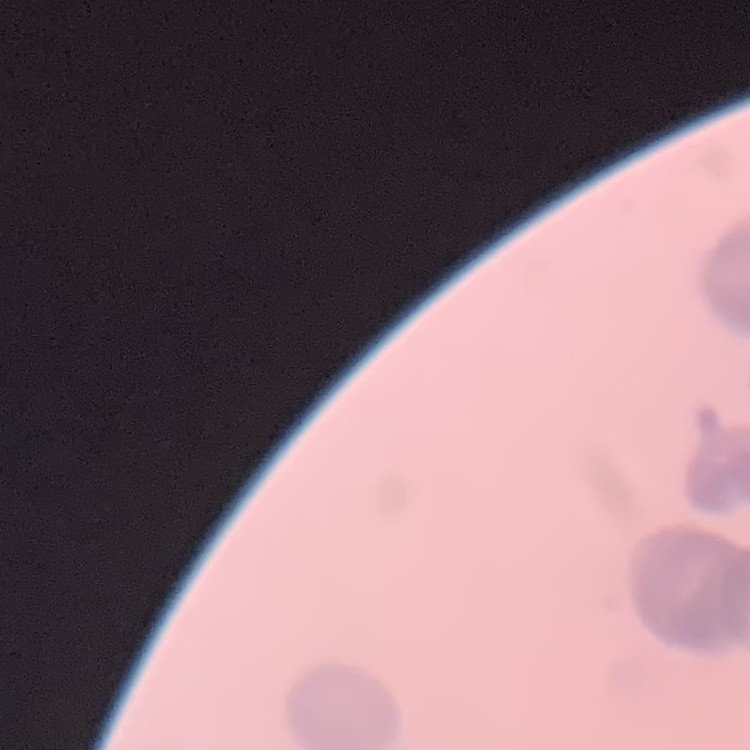

The erythrocytes show rouleaux formation. Thin blood film. Stained with either Field's or Giemsa. One tile cut from a larger photomicrograph.